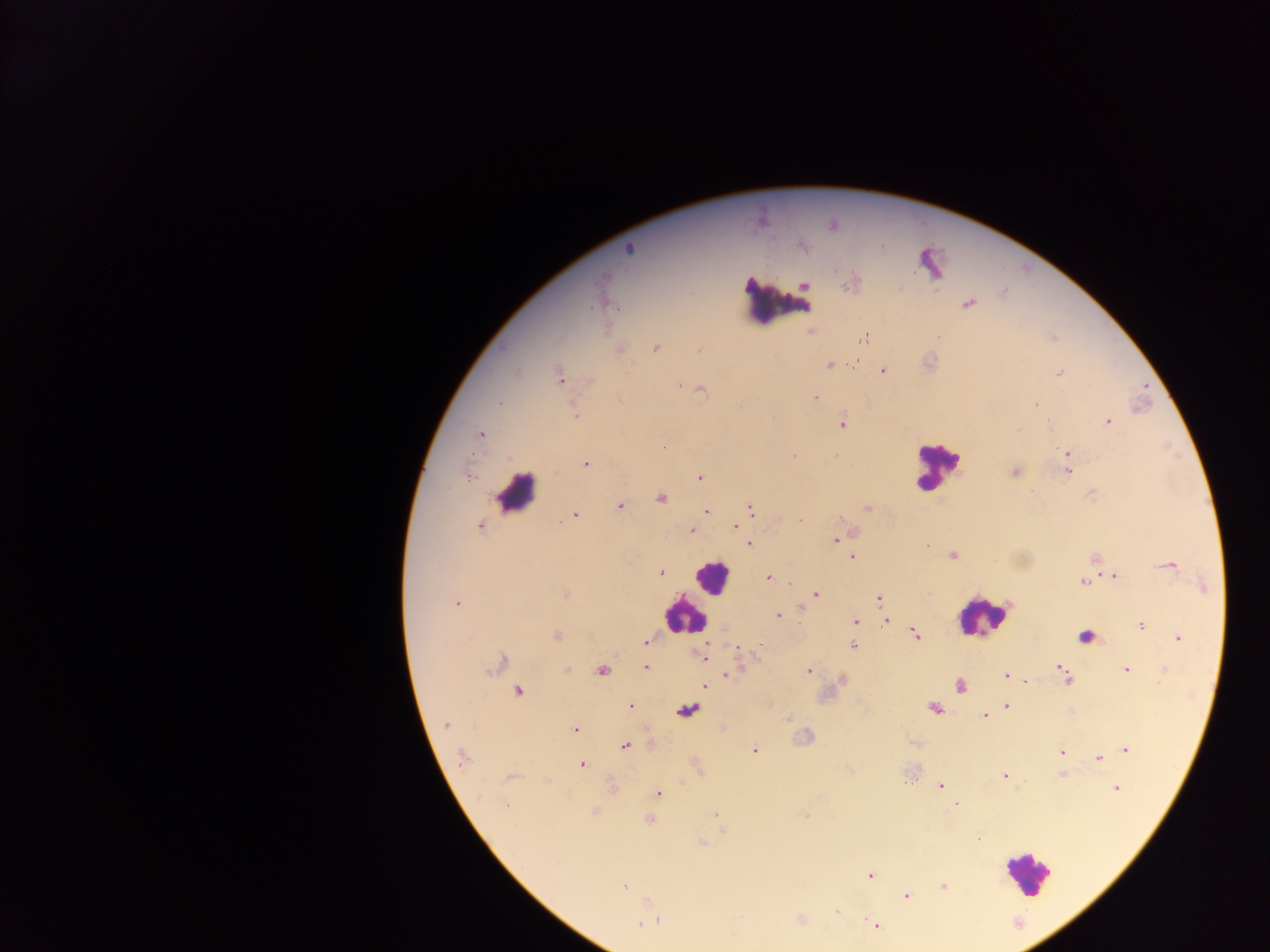
preparation = thick blood film
country = Ghana
Plasmodium parasite locations = approximate centers as (x, y) in pixels: (832, 225), (802, 246), (629, 249), (604, 278), (851, 284), (805, 285), (968, 303), (610, 304), (863, 339), (656, 348), (620, 350), (699, 350), (829, 365), (883, 371), (516, 372), (1060, 373), (560, 378), (679, 386), (702, 389), (815, 397), (498, 403), (1035, 404), (574, 414), (1108, 421), (1049, 423), (842, 424), (481, 434), (1067, 453), (794, 456), (586, 463), (1015, 472), (1067, 472), (468, 477), (700, 477), (661, 498), (620, 506), (867, 508), (750, 510), (706, 511), (574, 515), (741, 518), (800, 521), (480, 526), (736, 526), (691, 530), (835, 540), (749, 544), (952, 555), (852, 556), (1169, 565), (660, 573), (1114, 576), (768, 577), (1083, 582), (565, 593), (816, 595), (879, 599), (456, 603), (778, 616), (885, 621), (856, 622), (1141, 625), (916, 635), (556, 636), (1086, 636), (1178, 638), (645, 642), (853, 646), (703, 657), (502, 659), (646, 668), (1059, 668), (567, 669), (602, 670), (1126, 670), (808, 671), (1064, 672), (727, 675), (1006, 676), (1026, 681), (705, 685), (960, 686), (519, 691), (630, 706), (1007, 706), (934, 708), (687, 710), (985, 716), (445, 725), (574, 729), (624, 746), (1126, 749), (755, 751), (1062, 752), (463, 757), (1098, 758), (582, 764), (1004, 776), (511, 777), (905, 783), (941, 786), (1116, 788), (658, 793), (955, 804), (506, 805), (715, 815), (649, 820), (978, 839), (701, 842), (870, 875), (624, 887), (943, 887), (906, 896), (837, 911), (657, 921), (643, 923), (876, 926)
capture = mobile-phone photograph through a microscope
image size = 1270×952 pixels
field of view = single
leukocyte locations = approximate centers as (x, y) in pixels: (777, 299), (936, 465), (516, 493), (711, 576), (683, 615), (982, 616), (1026, 873)